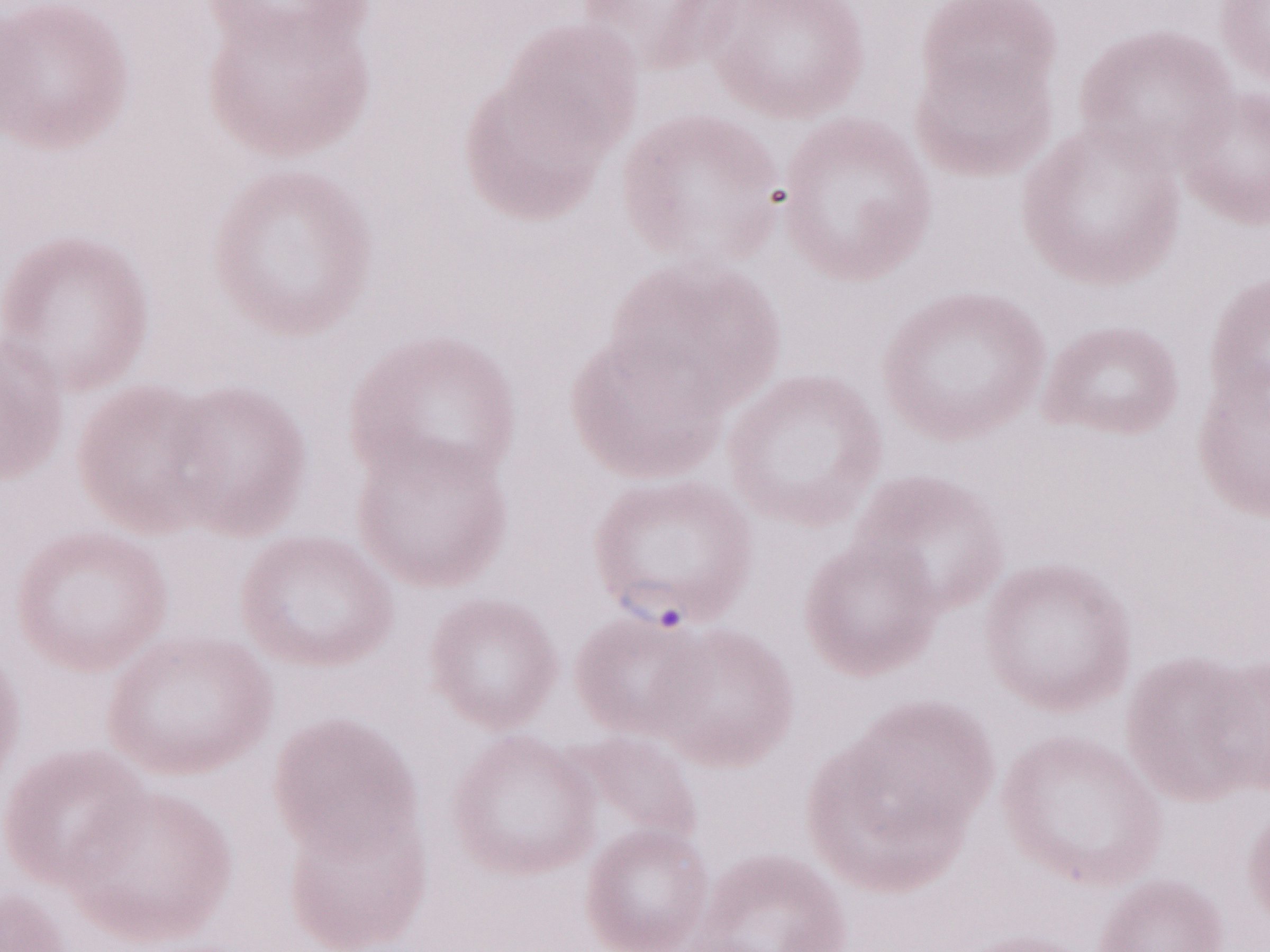

Patient diagnosis: malaria infection. Magnification: 1,000x. May-Grünwald-Giemsa-stained preparation. Thin peripheral-blood smear. Image is 1270×952 pixels. One field of this slide. Olympus BX43 microscope, Olympus DP73 camera.